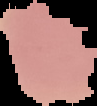
Summary:
  - Image type: cell region segmented out of the field of view; surrounding area masked to black
  - Preparation: thin blood film
  - Image size: 97×106 pixels
  - Result: negative for Plasmodium parasites